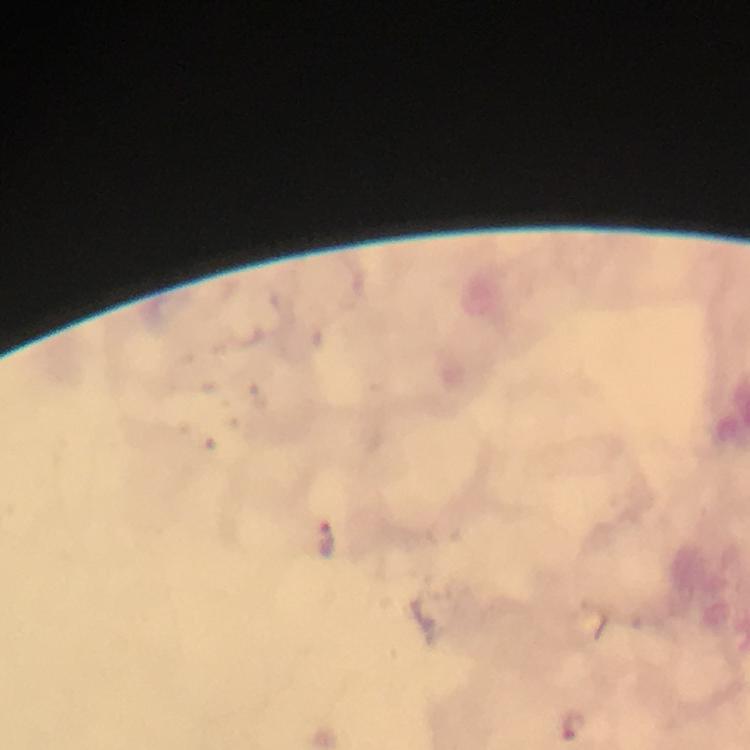 Approximate centers as {x, y} in pixels. Malaria parasite locations: {325, 539}, {571, 724}. At 100x magnification. Thick blood film. Image is 750×750 pixels. From a malaria diagnostic workup. Giemsa stain. Immersion oil was used. Cropped region of a single field of view. Photographed with a smartphone mounted on the microscope.